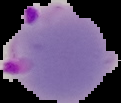 The area outside the segmented cell region is set to black. Image is 121×103 pixels. Result: malaria parasites detected. From a thin blood film.